Point out every Plasmodium parasite and every leukocyte.
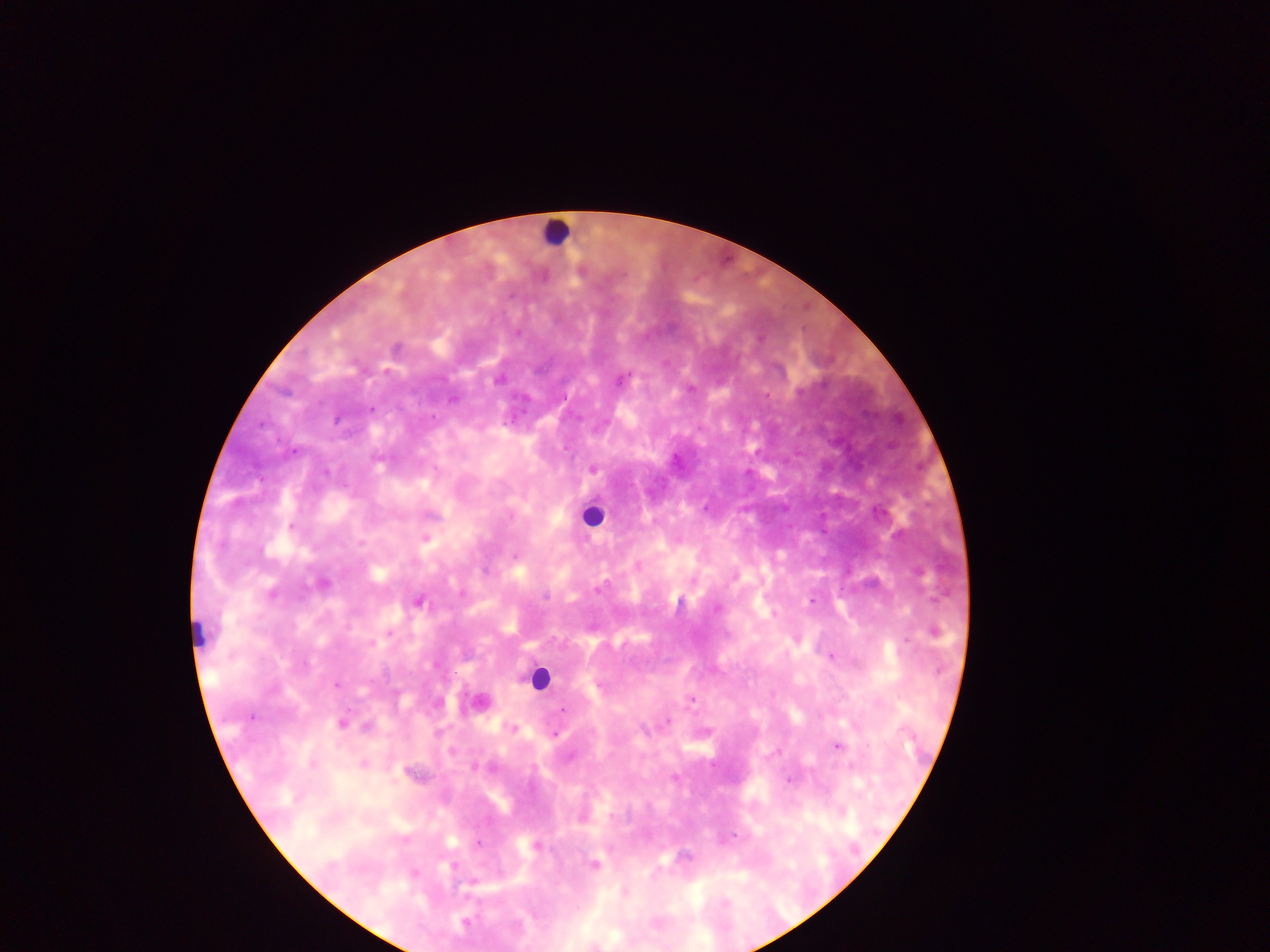
Approximate centers as [x, y] in pixels.
Plasmodium parasites: [498, 379], [453, 399], [371, 409], [336, 421], [294, 451], [593, 469], [325, 472], [705, 508], [291, 525], [426, 538], [514, 556], [271, 594], [545, 596], [812, 601], [419, 602], [717, 609], [933, 633], [372, 643], [831, 657], [335, 684], [691, 699], [562, 709], [251, 717], [668, 721], [341, 724], [513, 729], [555, 735], [838, 747], [313, 764], [364, 764], [790, 779], [734, 835], [477, 843], [593, 865], [453, 866], [414, 873], [473, 882], [464, 922].
Leukocytes: [554, 233], [590, 516], [198, 636], [537, 678].

image size = 1270×952 pixels
field of view = single
preparation = thick blood film
capture = mobile-phone photograph through a microscope
country = Ghana